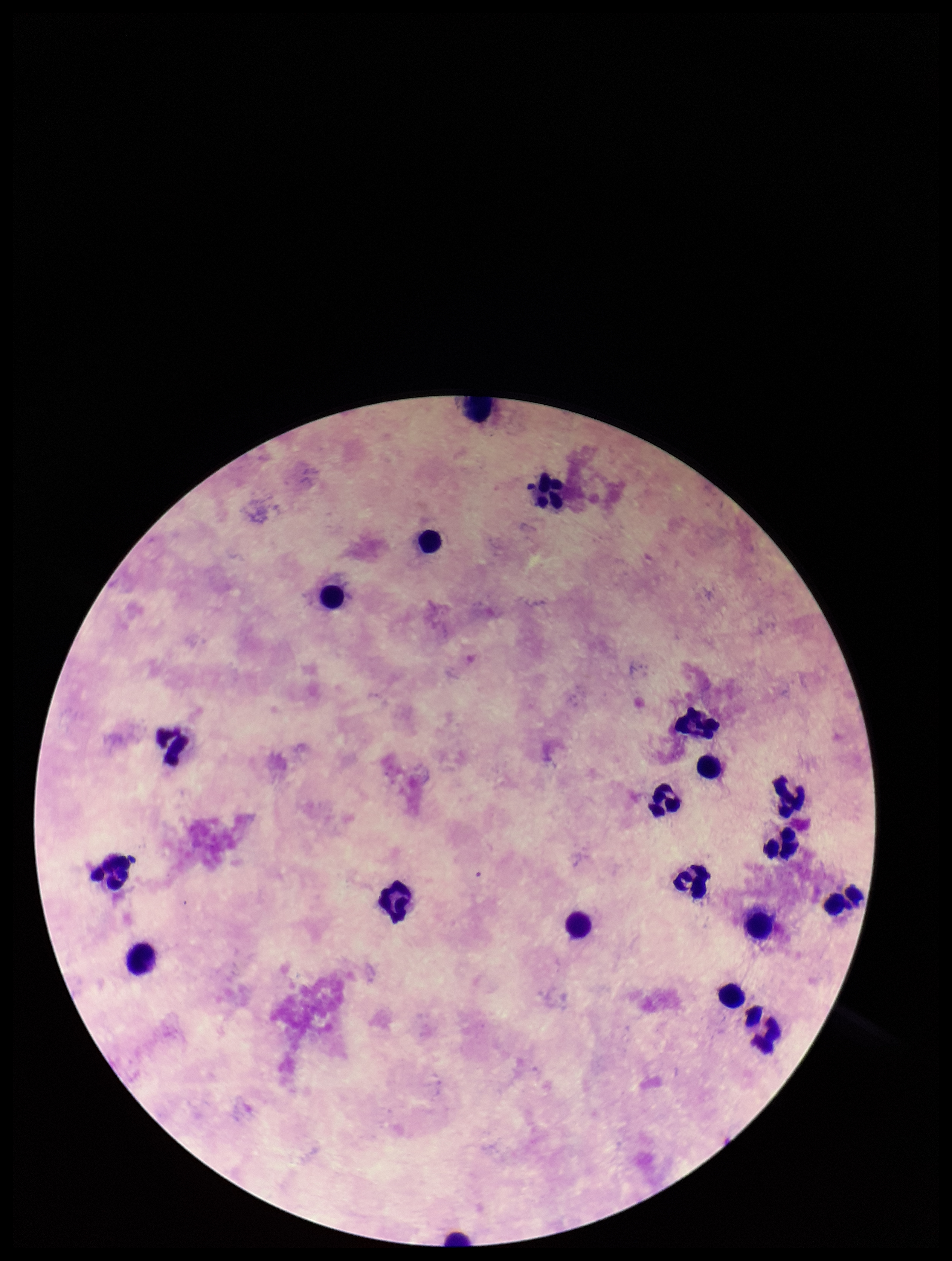
plasmodium_parasites: none seen
leukocyte_count: 21
preparation: thick smear
capture: smartphone photograph through the microscope eyepiece
field_of_view: one from this slide
parasite_count: 0
patient_malaria_status: negative
image_size: 952×1261 pixels
stain: Giemsa